State the blood parasite species.
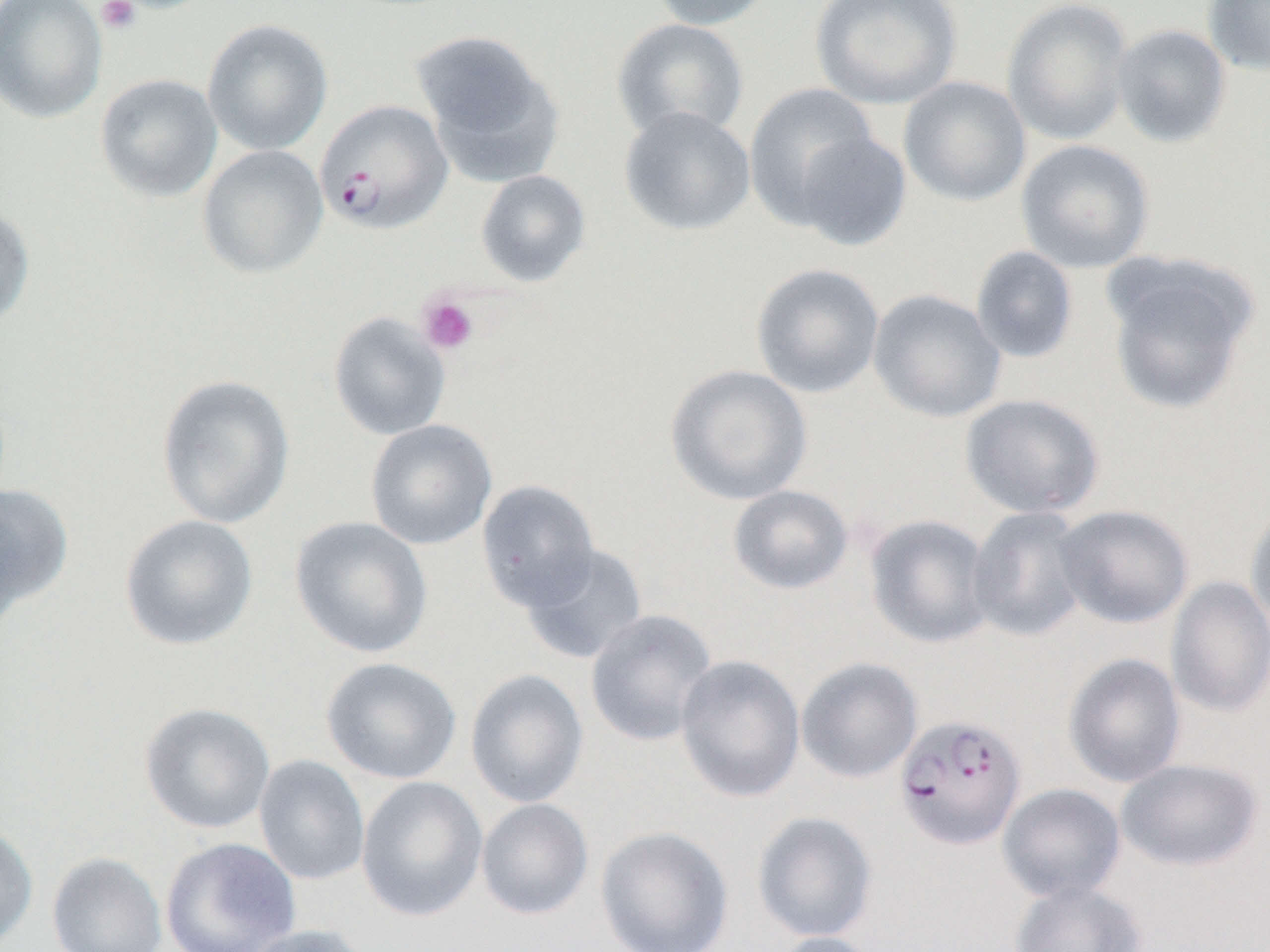

Plasmodium falciparum.

Summary:
  - Coordinate format: approximate bounding boxes as named x1/y1/x2/y2 corners in pixels
  - Uninfected red blood cell locations: (x1=0, y1=0, x2=108, y2=124), (x1=647, y1=0, x2=780, y2=31), (x1=810, y1=0, x2=963, y2=110), (x1=1002, y1=0, x2=1134, y2=146), (x1=1202, y1=0, x2=1270, y2=77), (x1=202, y1=18, x2=333, y2=156), (x1=611, y1=18, x2=750, y2=142), (x1=1111, y1=23, x2=1232, y2=148), (x1=411, y1=28, x2=566, y2=186), (x1=94, y1=73, x2=223, y2=203), (x1=898, y1=75, x2=1031, y2=207), (x1=744, y1=83, x2=881, y2=229), (x1=619, y1=106, x2=756, y2=237), (x1=792, y1=131, x2=913, y2=251), (x1=1016, y1=139, x2=1155, y2=273), (x1=197, y1=145, x2=329, y2=279), (x1=475, y1=169, x2=592, y2=287), (x1=0, y1=202, x2=35, y2=331), (x1=970, y1=245, x2=1079, y2=364), (x1=1102, y1=254, x2=1257, y2=415), (x1=750, y1=262, x2=885, y2=399), (x1=868, y1=288, x2=1007, y2=423), (x1=328, y1=311, x2=452, y2=441), (x1=664, y1=364, x2=813, y2=506), (x1=156, y1=374, x2=295, y2=529), (x1=960, y1=393, x2=1105, y2=520), (x1=365, y1=419, x2=498, y2=550), (x1=476, y1=479, x2=600, y2=612), (x1=0, y1=484, x2=74, y2=621), (x1=727, y1=485, x2=854, y2=595), (x1=1245, y1=500, x2=1270, y2=637), (x1=1054, y1=504, x2=1194, y2=629), (x1=966, y1=506, x2=1091, y2=643), (x1=119, y1=514, x2=258, y2=651), (x1=864, y1=514, x2=996, y2=649), (x1=289, y1=517, x2=434, y2=659), (x1=519, y1=542, x2=650, y2=666), (x1=1165, y1=576, x2=1270, y2=718), (x1=585, y1=609, x2=718, y2=747), (x1=1062, y1=653, x2=1187, y2=788), (x1=675, y1=654, x2=806, y2=803), (x1=321, y1=657, x2=462, y2=785), (x1=797, y1=657, x2=923, y2=783), (x1=465, y1=668, x2=589, y2=808), (x1=139, y1=702, x2=276, y2=834), (x1=253, y1=754, x2=370, y2=886), (x1=1115, y1=758, x2=1263, y2=872), (x1=356, y1=776, x2=488, y2=923), (x1=997, y1=783, x2=1126, y2=903), (x1=475, y1=798, x2=594, y2=920), (x1=752, y1=811, x2=878, y2=943), (x1=0, y1=821, x2=38, y2=950), (x1=595, y1=826, x2=734, y2=952), (x1=160, y1=837, x2=300, y2=952), (x1=47, y1=851, x2=168, y2=952), (x1=1008, y1=880, x2=1148, y2=952), (x1=238, y1=924, x2=374, y2=952), (x1=769, y1=932, x2=885, y2=952)
  - Plasmodium falciparum-infected red blood cell locations: (x1=314, y1=99, x2=453, y2=235), (x1=894, y1=713, x2=1027, y2=850)
  - Platelet locations: (x1=96, y1=0, x2=141, y2=34), (x1=417, y1=292, x2=479, y2=355)
  - Field of view: one of a larger specimen
  - Magnification: 1000x
  - Preparation: thin blood smear
  - Image size: 1270×952 pixels
  - Modality: optical microscopy